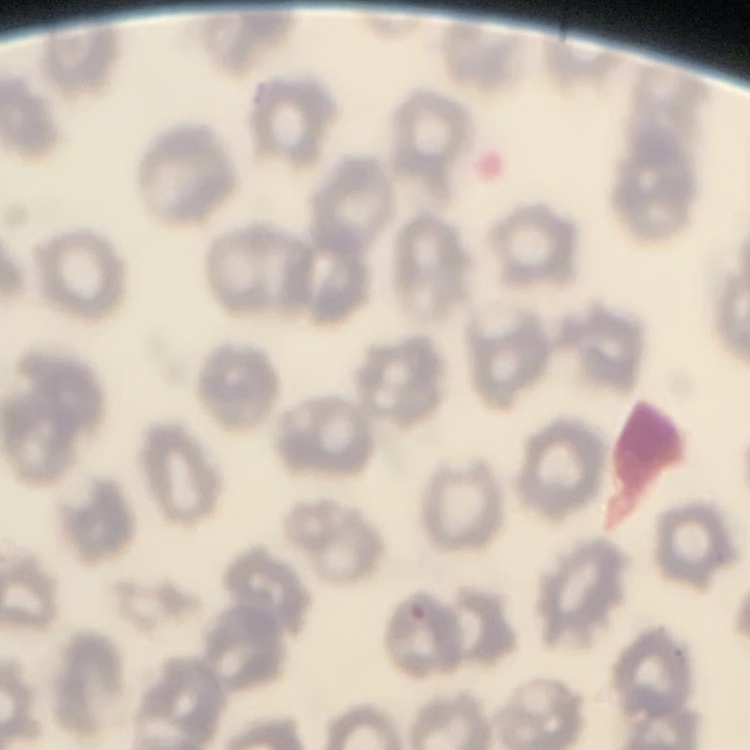
Summary:
  - Erythrocyte morphology: no rouleaux formation
  - Image type: square crop of a larger photomicrograph
  - Preparation: thin blood smear
  - Stain: Field's or Giemsa